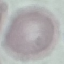

Summary:
  - Malaria status: uninfected
  - Image type: cell patch, automatically extracted from a larger field of view and resized to 64 × 64 pixels
  - Capture: smartphone camera at the microscope eyepiece
  - Stain: Giemsa
  - Preparation: thin smear